Locate every Plasmodium vivax-infected red blood cell.
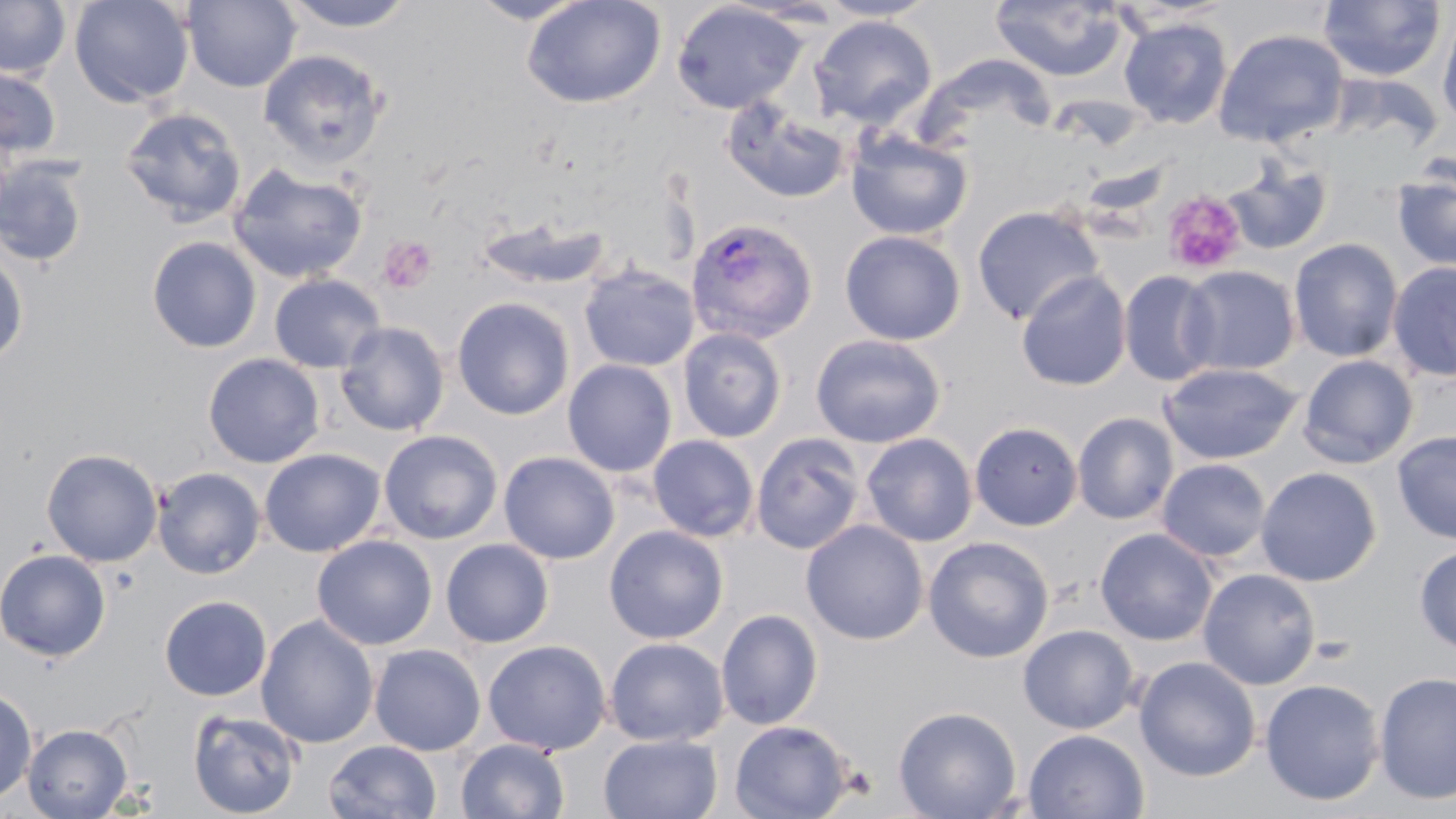

Approximate bounding boxes as named x1/y1/x2/y2 corners in pixels.
Plasmodium vivax-infected red blood cells: (x1=685, y1=217, x2=818, y2=345).

Summary:
  - Platelet locations: (x1=1161, y1=190, x2=1248, y2=276), (x1=378, y1=235, x2=437, y2=294)
  - Uninfected red blood cell locations: (x1=70, y1=0, x2=194, y2=107), (x1=279, y1=0, x2=419, y2=32), (x1=467, y1=0, x2=592, y2=24), (x1=522, y1=0, x2=666, y2=109), (x1=815, y1=0, x2=938, y2=21), (x1=1318, y1=0, x2=1446, y2=82), (x1=0, y1=1, x2=71, y2=79), (x1=182, y1=1, x2=302, y2=92), (x1=990, y1=1, x2=1129, y2=81), (x1=671, y1=2, x2=807, y2=114), (x1=1438, y1=10, x2=1456, y2=134), (x1=809, y1=15, x2=937, y2=129), (x1=1119, y1=17, x2=1233, y2=129), (x1=1213, y1=29, x2=1350, y2=148), (x1=259, y1=49, x2=388, y2=168), (x1=0, y1=63, x2=62, y2=161), (x1=721, y1=96, x2=851, y2=205), (x1=119, y1=107, x2=246, y2=227), (x1=135, y1=109, x2=253, y2=352), (x1=845, y1=127, x2=973, y2=241), (x1=0, y1=157, x2=90, y2=268), (x1=1221, y1=157, x2=1334, y2=256), (x1=228, y1=162, x2=369, y2=284), (x1=1392, y1=164, x2=1456, y2=272), (x1=972, y1=205, x2=1105, y2=325), (x1=475, y1=214, x2=611, y2=291), (x1=839, y1=229, x2=966, y2=346), (x1=147, y1=236, x2=262, y2=353), (x1=1288, y1=238, x2=1403, y2=362), (x1=0, y1=251, x2=29, y2=368), (x1=1387, y1=261, x2=1456, y2=382), (x1=579, y1=263, x2=700, y2=372), (x1=1178, y1=265, x2=1300, y2=376), (x1=1016, y1=270, x2=1132, y2=391), (x1=1118, y1=270, x2=1222, y2=387), (x1=268, y1=274, x2=386, y2=373), (x1=451, y1=297, x2=575, y2=420), (x1=335, y1=321, x2=449, y2=436), (x1=677, y1=327, x2=787, y2=443), (x1=810, y1=333, x2=946, y2=448), (x1=203, y1=353, x2=325, y2=468), (x1=1298, y1=354, x2=1419, y2=469), (x1=562, y1=359, x2=678, y2=477), (x1=1159, y1=362, x2=1303, y2=465), (x1=1072, y1=412, x2=1179, y2=525), (x1=969, y1=422, x2=1084, y2=531), (x1=378, y1=430, x2=503, y2=545), (x1=1393, y1=431, x2=1456, y2=544), (x1=861, y1=432, x2=978, y2=546), (x1=750, y1=433, x2=866, y2=554), (x1=648, y1=435, x2=760, y2=542), (x1=41, y1=448, x2=163, y2=567), (x1=259, y1=448, x2=386, y2=558), (x1=498, y1=451, x2=620, y2=564), (x1=1157, y1=458, x2=1271, y2=563), (x1=152, y1=467, x2=266, y2=579), (x1=1256, y1=467, x2=1382, y2=587), (x1=801, y1=520, x2=929, y2=645), (x1=604, y1=525, x2=729, y2=644), (x1=1095, y1=528, x2=1218, y2=646), (x1=312, y1=535, x2=438, y2=650), (x1=923, y1=536, x2=1054, y2=663), (x1=440, y1=539, x2=554, y2=648), (x1=1414, y1=544, x2=1456, y2=653), (x1=0, y1=548, x2=111, y2=661), (x1=1197, y1=568, x2=1321, y2=689), (x1=159, y1=595, x2=272, y2=701), (x1=715, y1=608, x2=823, y2=730), (x1=256, y1=615, x2=379, y2=749), (x1=1018, y1=624, x2=1139, y2=733), (x1=604, y1=637, x2=729, y2=747), (x1=483, y1=639, x2=611, y2=756), (x1=369, y1=643, x2=486, y2=756), (x1=1134, y1=656, x2=1261, y2=782), (x1=1373, y1=671, x2=1456, y2=804), (x1=1259, y1=678, x2=1385, y2=805), (x1=0, y1=686, x2=37, y2=805), (x1=893, y1=705, x2=1022, y2=819), (x1=187, y1=709, x2=302, y2=818), (x1=729, y1=719, x2=854, y2=818), (x1=22, y1=723, x2=132, y2=818), (x1=1023, y1=729, x2=1149, y2=818), (x1=598, y1=733, x2=723, y2=819), (x1=456, y1=738, x2=570, y2=819), (x1=324, y1=740, x2=442, y2=819)
  - Slide-level diagnosis: Plasmodium vivax
  - Preparation: thin blood smear
  - Magnification: 1000x
  - Stain: May-Grünwald-Giemsa
  - Image size: 1456×819 pixels
  - Field of view: one of a larger specimen
  - Modality: light microscopy